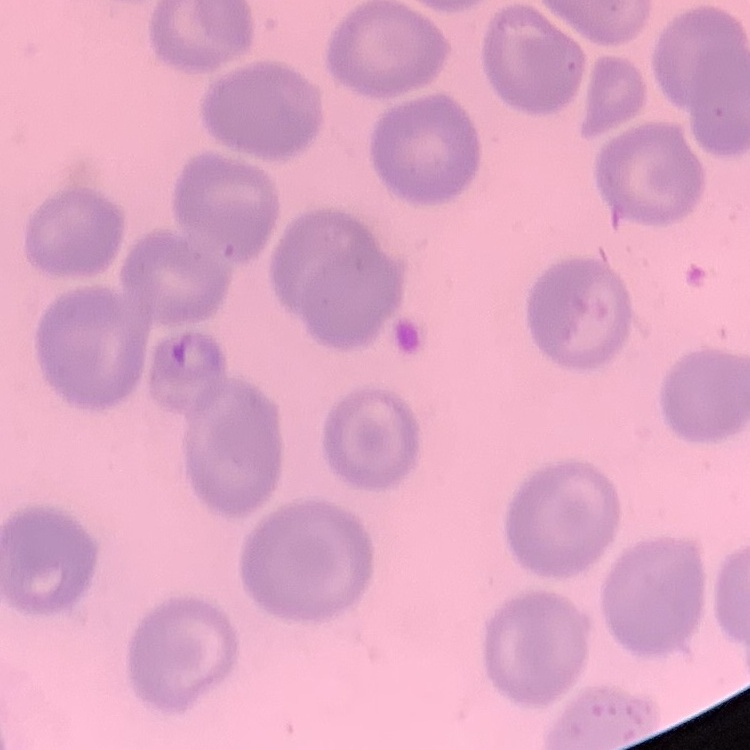
The red blood cells show no rouleaux formation. Stained with either Field's or Giemsa. Square crop of a larger photomicrograph. Thin blood film.